State which parasite is depicted.
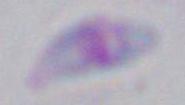
Toxoplasma gondii.

1000x magnification. Photomicrograph.